Identify the parasite.
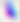

This is Toxoplasma gondii.

Summary:
  - Modality: micrograph
  - Magnification: 400x